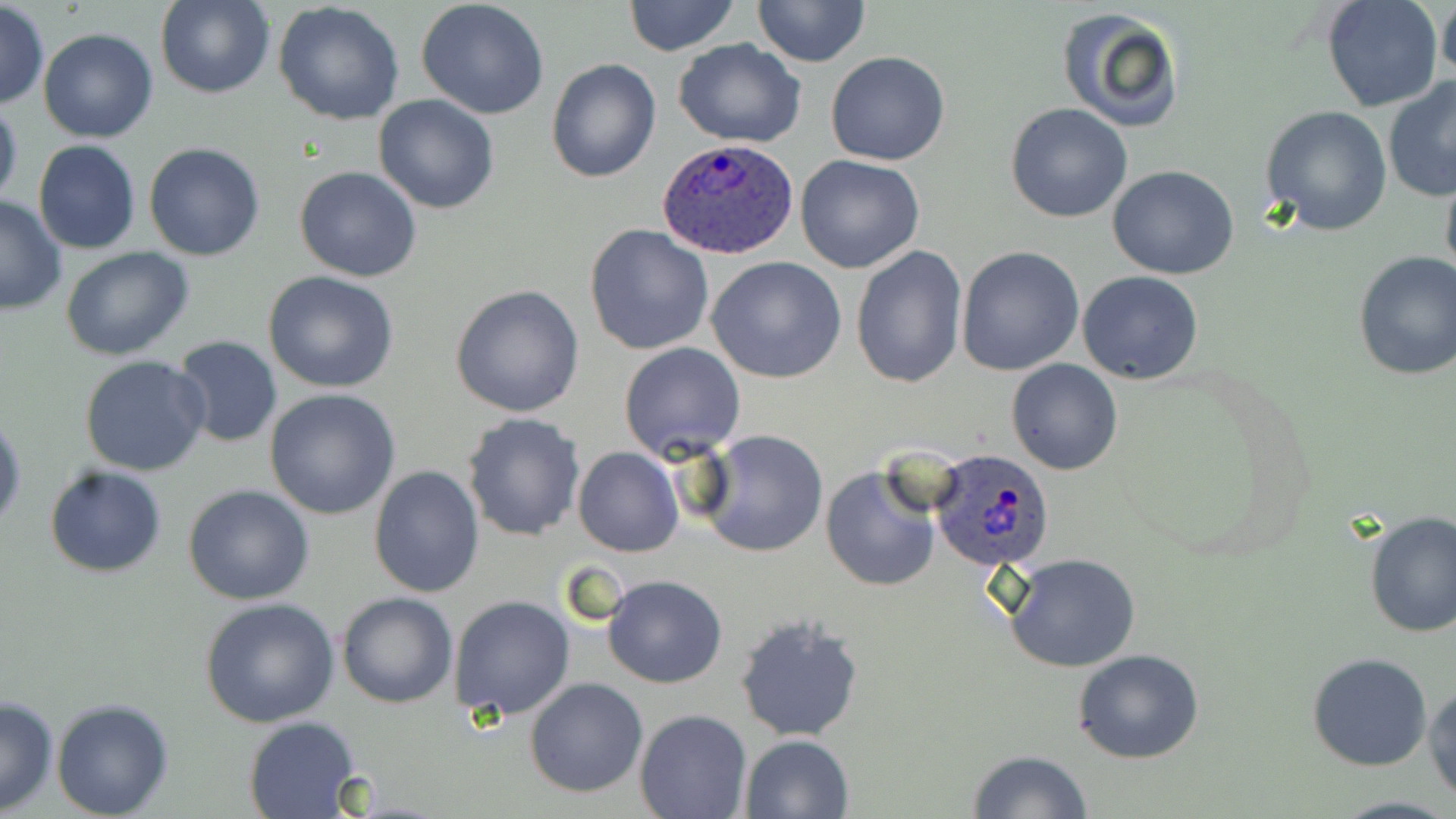

slide-level diagnosis = Plasmodium ovale
stain = May-Grünwald-Giemsa
preparation = thin blood film
Plasmodium ovale-infected red blood cell locations = approximate bounding boxes as named x1/y1/x2/y2 corners in pixels: (x1=658, y1=136, x2=800, y2=259), (x1=928, y1=450, x2=1056, y2=572)
modality = light microscopy
image size = 1456×819 pixels
magnification = 1000x
field of view = single
uninfected red blood cell locations = approximate bounding boxes as named x1/y1/x2/y2 corners in pixels: (x1=154, y1=0, x2=275, y2=99), (x1=623, y1=0, x2=741, y2=57), (x1=752, y1=0, x2=870, y2=68), (x1=1320, y1=0, x2=1444, y2=114), (x1=1437, y1=0, x2=1456, y2=87), (x1=416, y1=1, x2=549, y2=119), (x1=273, y1=2, x2=404, y2=125), (x1=0, y1=3, x2=48, y2=108), (x1=1056, y1=5, x2=1186, y2=134), (x1=38, y1=28, x2=159, y2=144), (x1=673, y1=39, x2=805, y2=148), (x1=827, y1=51, x2=950, y2=166), (x1=546, y1=58, x2=661, y2=183), (x1=1383, y1=77, x2=1456, y2=202), (x1=373, y1=93, x2=500, y2=214), (x1=0, y1=96, x2=22, y2=212), (x1=1005, y1=103, x2=1132, y2=222), (x1=1261, y1=105, x2=1393, y2=235), (x1=33, y1=140, x2=141, y2=254), (x1=143, y1=142, x2=267, y2=261), (x1=794, y1=155, x2=925, y2=274), (x1=1440, y1=164, x2=1456, y2=291), (x1=294, y1=165, x2=421, y2=281), (x1=1107, y1=166, x2=1241, y2=278), (x1=0, y1=195, x2=67, y2=314), (x1=584, y1=223, x2=716, y2=356), (x1=850, y1=245, x2=968, y2=390), (x1=955, y1=245, x2=1084, y2=376), (x1=60, y1=246, x2=195, y2=360), (x1=1352, y1=250, x2=1456, y2=381), (x1=707, y1=257, x2=847, y2=384), (x1=1078, y1=270, x2=1204, y2=385), (x1=263, y1=271, x2=401, y2=393), (x1=450, y1=283, x2=585, y2=417), (x1=171, y1=336, x2=283, y2=450), (x1=618, y1=341, x2=746, y2=460), (x1=79, y1=355, x2=211, y2=477), (x1=1006, y1=358, x2=1122, y2=475), (x1=265, y1=388, x2=402, y2=520), (x1=0, y1=409, x2=25, y2=534), (x1=461, y1=411, x2=587, y2=541), (x1=697, y1=429, x2=828, y2=558), (x1=573, y1=447, x2=682, y2=556), (x1=44, y1=464, x2=167, y2=578), (x1=819, y1=464, x2=942, y2=593), (x1=368, y1=466, x2=485, y2=596), (x1=183, y1=484, x2=314, y2=605), (x1=1361, y1=509, x2=1455, y2=640), (x1=1004, y1=554, x2=1141, y2=673), (x1=603, y1=575, x2=728, y2=688), (x1=337, y1=591, x2=457, y2=708), (x1=448, y1=594, x2=576, y2=720), (x1=199, y1=597, x2=339, y2=728), (x1=733, y1=614, x2=864, y2=743), (x1=1072, y1=648, x2=1207, y2=764), (x1=1306, y1=652, x2=1434, y2=771), (x1=524, y1=677, x2=648, y2=798), (x1=1423, y1=682, x2=1456, y2=801), (x1=0, y1=694, x2=60, y2=816), (x1=50, y1=697, x2=173, y2=818), (x1=635, y1=710, x2=751, y2=819), (x1=242, y1=715, x2=361, y2=817), (x1=739, y1=735, x2=854, y2=819), (x1=968, y1=748, x2=1094, y2=818), (x1=1327, y1=794, x2=1456, y2=819)